Assess this cell for malaria.
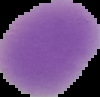
It is uninfected.

Summary:
  - Image type: segmented cell region with the area outside set to black
  - Image size: 100×97 pixels
  - Preparation: thin blood smear